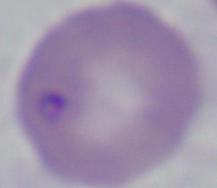 Micrograph. Captured at 1000x magnification. A Babesia parasite is seen.